Comment on the morphology of the red blood cells.
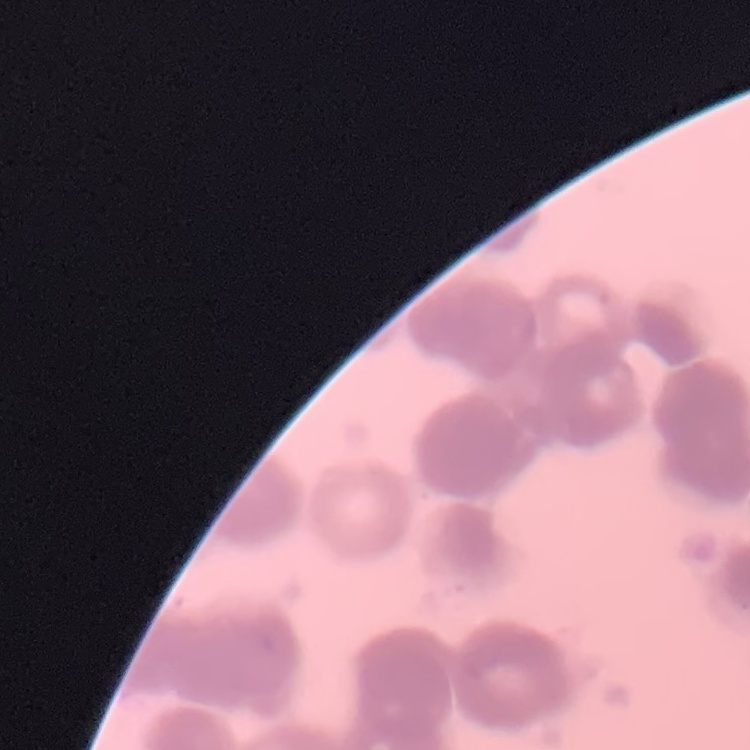
Rouleaux formation.

{
  "stain": "Field's or Giemsa",
  "preparation": "thin peripheral smear",
  "image_type": "square crop of a larger photomicrograph"
}